Locate every blood parasite and identify its species.
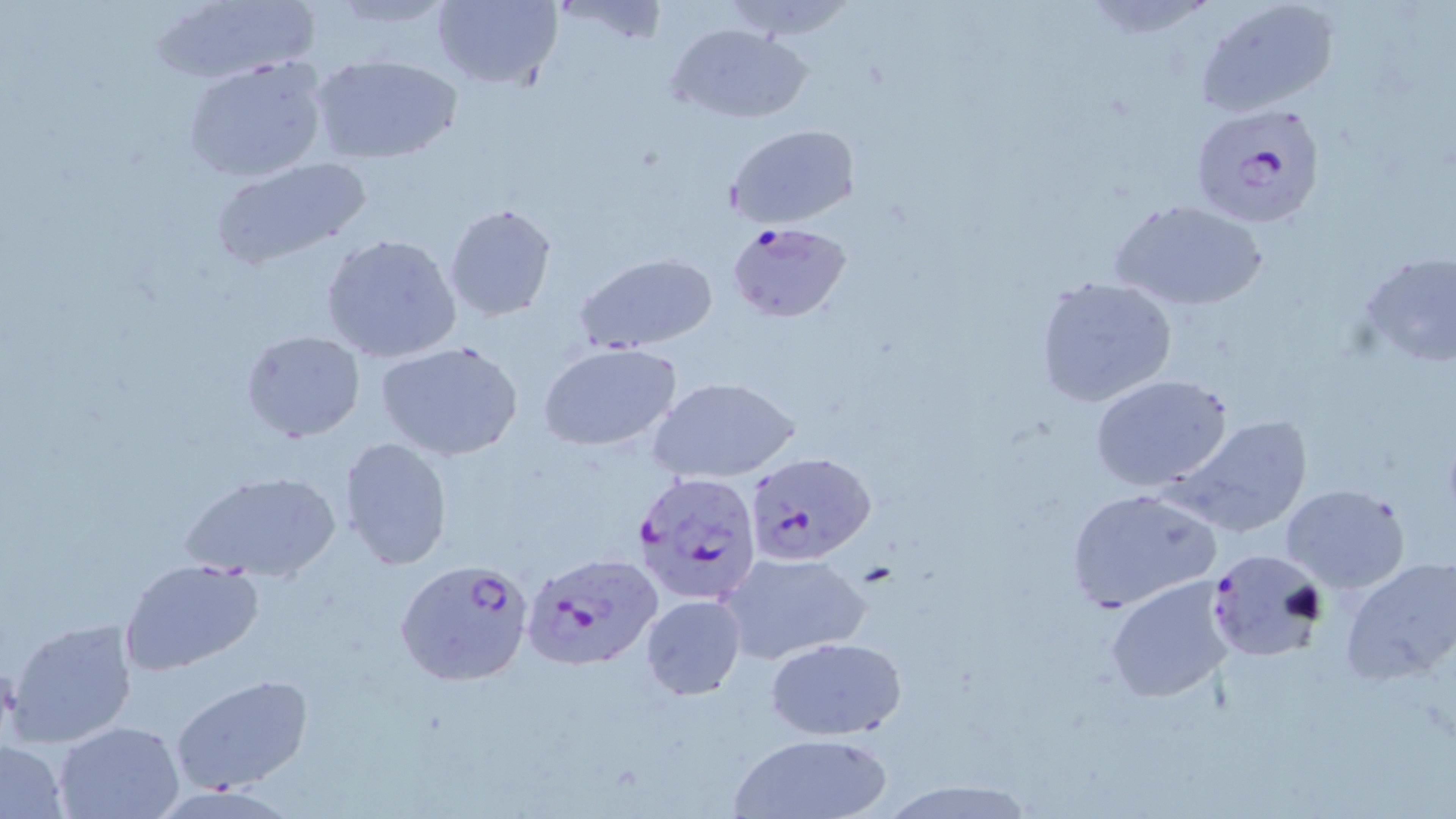
Approximate bounding boxes as [x1, y1, x2, y2] in pixels.
Plasmodium falciparum-infected red blood cells: [1189, 102, 1328, 231], [728, 220, 854, 324], [745, 450, 876, 567], [632, 470, 765, 606], [1206, 548, 1326, 665], [522, 551, 663, 672], [396, 558, 536, 688].
No Plasmodium ovale, Plasmodium malariae, Plasmodium vivax, Babesia divergens, or Trypanosoma brucei observed.

slide-level diagnosis = Plasmodium falciparum
field of view = one of a larger specimen
magnification = 1000x
stain = May-Grünwald-Giemsa
modality = optical microscopy
preparation = thin blood smear
uninfected red blood cell locations = approximate bounding boxes as [x1, y1, x2, y2] in pixels: [430, 0, 563, 91], [718, 0, 855, 40], [1195, 0, 1340, 117], [149, 2, 321, 84], [666, 22, 811, 124], [183, 51, 330, 179], [312, 55, 460, 164], [725, 123, 859, 230], [210, 155, 374, 268], [1111, 199, 1267, 312], [444, 202, 558, 321], [321, 234, 462, 363], [1358, 251, 1456, 372], [574, 252, 720, 353], [1034, 275, 1178, 408], [241, 329, 366, 443], [378, 342, 523, 462], [538, 343, 681, 451], [1091, 375, 1236, 492], [648, 376, 802, 483], [1165, 414, 1315, 538], [338, 436, 453, 571], [182, 469, 342, 585], [1280, 483, 1410, 593], [1063, 487, 1221, 615], [719, 550, 871, 664], [1338, 554, 1456, 686], [119, 558, 265, 676], [1104, 575, 1241, 704], [640, 595, 746, 697], [5, 617, 139, 747], [764, 636, 908, 741], [170, 674, 315, 794], [55, 720, 187, 818], [729, 731, 892, 818], [0, 740, 69, 818]
image size = 1456×819 pixels